Locate every leukocyte (white blood cell).
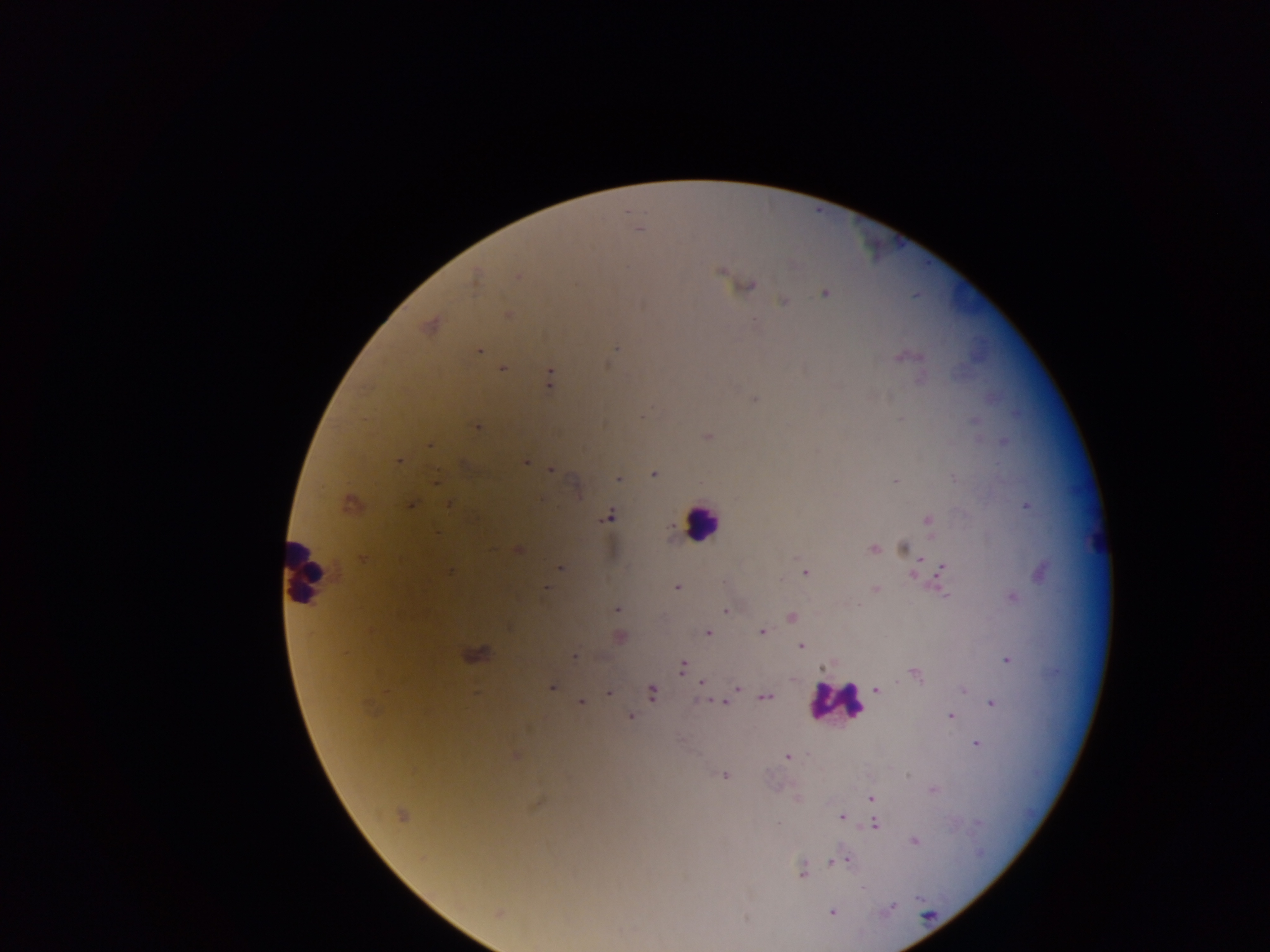
Approximate centers as x y in pixels.
Leukocytes: 700 521; 306 572; 836 701.

Plasmodium parasite locations: 638 228; 722 270; 518 276; 475 277; 574 283; 748 285; 824 292; 783 301; 508 315; 429 325; 618 346; 478 350; 904 356; 503 368; 549 379; 755 399; 477 426; 708 435; 429 444; 398 461; 526 461; 551 470; 654 473; 619 479; 436 480; 895 480; 350 503; 411 504; 450 505; 1026 505; 608 516; 926 519; 671 529; 903 548; 517 550; 872 550; 362 558; 560 567; 942 570; 448 571; 1041 571; 805 573; 914 573; 676 586; 545 588; 875 590; 1011 597; 616 609; 725 611; 791 616; 707 631; 762 631; 619 637; 801 646; 475 654; 574 656; 1006 660; 683 666; 823 668; 915 674; 702 683; 551 687; 737 687; 876 690; 963 690; 652 692; 608 693; 765 696; 712 700; 582 702; 726 702; 991 702; 630 716; 949 716; 976 743; 516 755; 787 756; 724 775; 932 789; 870 798; 796 799; 536 803; 401 815; 842 817; 875 824; 914 841; 834 860; 846 860; 801 872; 831 912; 498 913. Photographed through a microscope with a mobile-phone camera. Collected in Ghana. Single field of view. Thick blood film. Image is 1270×952 pixels.